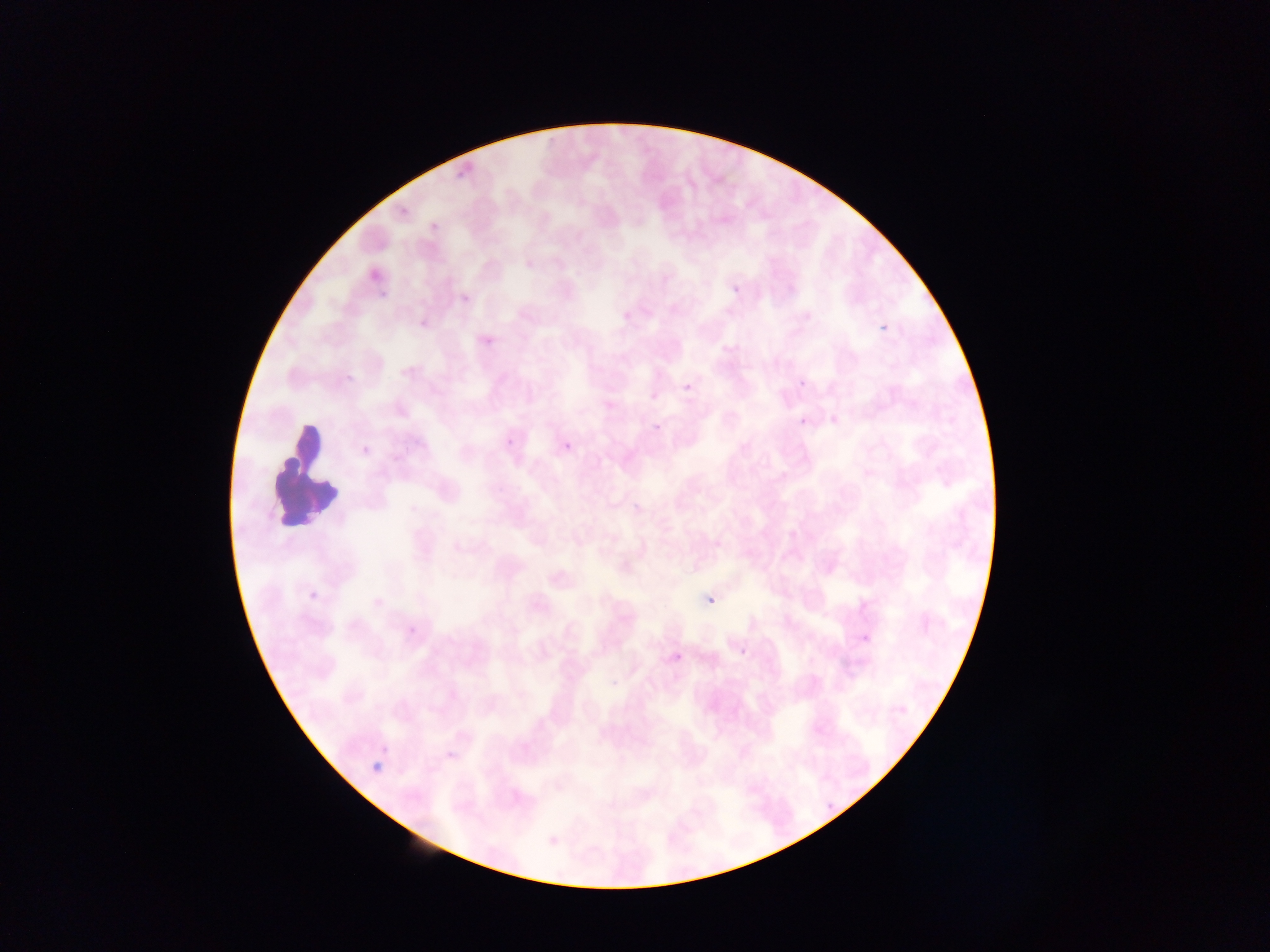
{
  "preparation": "thin blood smear",
  "field_of_view": "single",
  "country": "Ghana",
  "capture": "mobile-phone photograph through a microscope",
  "image_size": "1270×952 pixels",
  "leukocyte_locations": "approximate bounding boxes as [left, top, right, bottom] in pixels: [246, 423, 337, 536]",
  "plasmodium_parasite_locations": "approximate bounding boxes as [left, top, right, bottom] in pixels: [451, 147, 498, 185], [373, 277, 404, 297], [731, 284, 740, 294], [412, 310, 436, 331], [880, 322, 888, 331], [483, 335, 495, 346], [338, 367, 360, 385], [795, 378, 803, 389], [675, 379, 690, 399], [793, 411, 815, 432], [643, 417, 663, 436], [502, 437, 517, 444], [349, 441, 381, 458], [563, 442, 572, 451], [305, 576, 333, 602], [705, 589, 723, 606], [407, 623, 418, 635], [846, 628, 884, 653], [717, 645, 748, 665], [672, 652, 683, 662], [819, 736, 857, 758], [367, 757, 389, 777], [821, 784, 856, 821], [548, 837, 558, 847]"
}